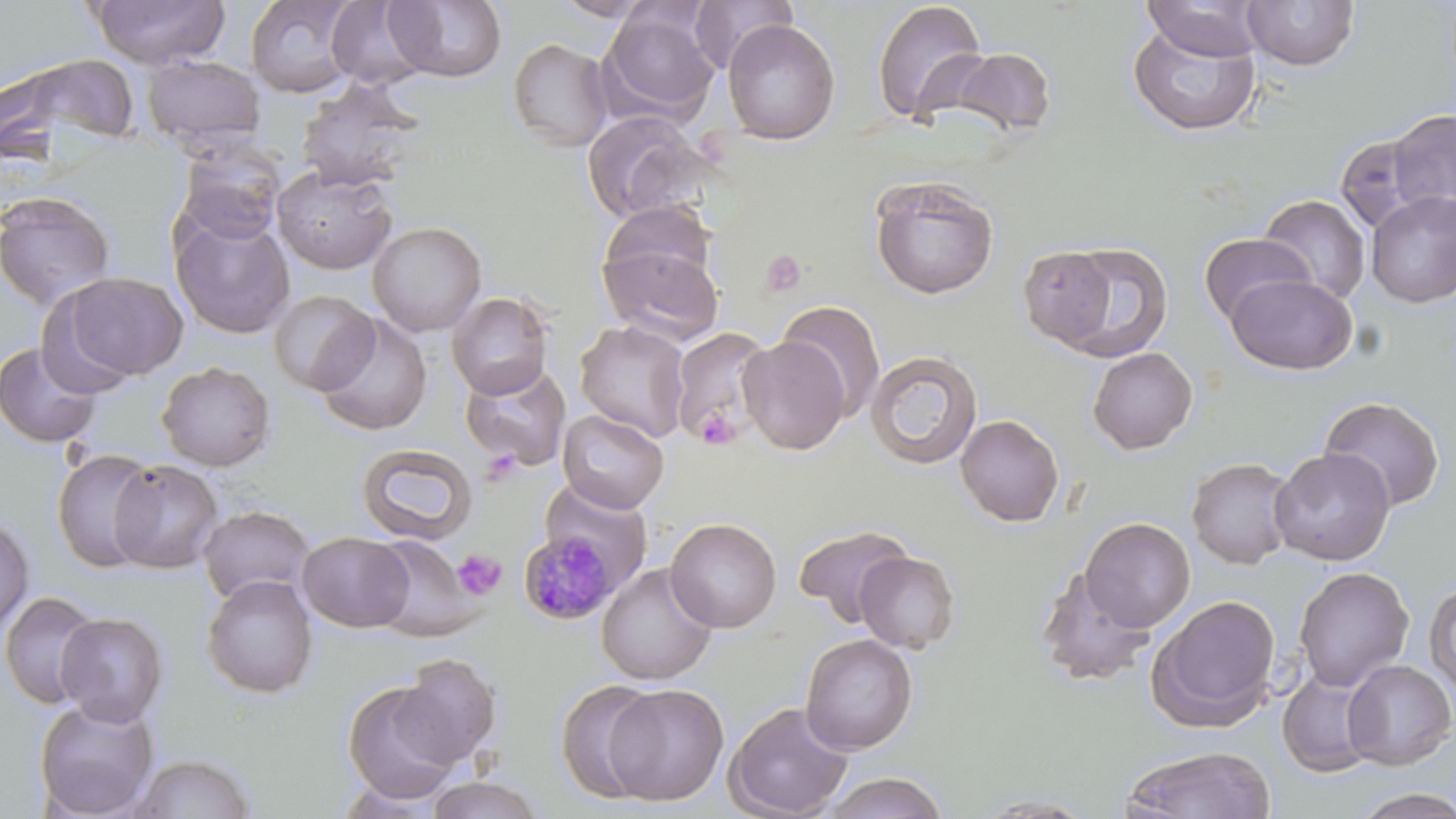
slide_level_diagnosis: Plasmodium malariae
magnification: 1000x
field_of_view: single
platelet_locations: 'approximate bounding boxes as (x1, y1, x2, y2) in pixels: (760, 250, 809, 297), (696, 408, 740, 449), (452, 550, 506, 600)'
stain: May-Grünwald-Giemsa
uninfected_red_blood_cell_locations: 'approximate bounding boxes as (x1, y1, x2, y2) in pixels: (88, 0, 229, 69), (326, 0, 429, 89), (549, 0, 661, 21), (689, 0, 797, 73), (1242, 0, 1359, 72), (245, 1, 362, 98), (383, 1, 508, 83), (870, 1, 990, 127), (1140, 1, 1265, 61), (599, 7, 721, 125), (721, 18, 840, 146), (1127, 21, 1262, 137), (508, 37, 614, 153), (953, 47, 1056, 139), (1, 52, 140, 165), (141, 54, 267, 153), (295, 77, 427, 192), (1386, 108, 1456, 218), (581, 110, 709, 224), (1335, 131, 1434, 236), (174, 143, 286, 245), (272, 165, 398, 275), (869, 175, 1000, 300), (0, 190, 117, 311), (1366, 191, 1456, 307), (1258, 194, 1371, 306), (597, 200, 718, 301), (170, 212, 296, 340), (367, 221, 487, 337), (1199, 233, 1314, 328), (598, 241, 724, 345), (1049, 241, 1174, 362), (1017, 244, 1120, 350), (57, 272, 189, 381), (1225, 272, 1358, 375), (267, 289, 378, 395), (446, 292, 554, 399), (774, 299, 887, 420), (313, 314, 433, 436), (574, 320, 691, 443), (668, 326, 775, 447), (737, 336, 851, 454), (1, 342, 103, 448), (1087, 347, 1198, 454), (865, 350, 984, 470), (459, 360, 572, 471), (157, 361, 276, 471), (1319, 396, 1446, 512), (557, 409, 670, 513), (955, 414, 1064, 527), (356, 443, 478, 546), (1268, 447, 1395, 565), (51, 449, 160, 574), (1186, 457, 1297, 570), (109, 459, 223, 573), (538, 478, 654, 599), (198, 505, 317, 606), (0, 515, 35, 635), (665, 517, 782, 633), (1080, 517, 1195, 632), (793, 523, 914, 625), (298, 531, 413, 632), (367, 534, 484, 641), (854, 551, 962, 654), (596, 563, 718, 685), (1033, 566, 1156, 689), (1293, 566, 1415, 692), (202, 574, 319, 699), (1424, 581, 1456, 694), (1, 590, 104, 709), (1148, 594, 1282, 729), (55, 611, 169, 726), (800, 633, 918, 755), (392, 653, 502, 768), (1341, 660, 1456, 771), (1277, 668, 1381, 778), (341, 680, 464, 803), (555, 680, 665, 804), (602, 683, 730, 806), (33, 696, 160, 817), (723, 701, 854, 819), (1120, 745, 1277, 819), (128, 752, 259, 818), (821, 771, 949, 819), (422, 775, 548, 818), (1349, 788, 1456, 818), (970, 793, 1103, 817)'
plasmodium_malariae_infected_red_blood_cell_locations: 'approximate bounding boxes as (x1, y1, x2, y2) in pixels: (518, 530, 624, 625)'
modality: optical microscopy
image_size: 1456×819 pixels
preparation: thin blood film